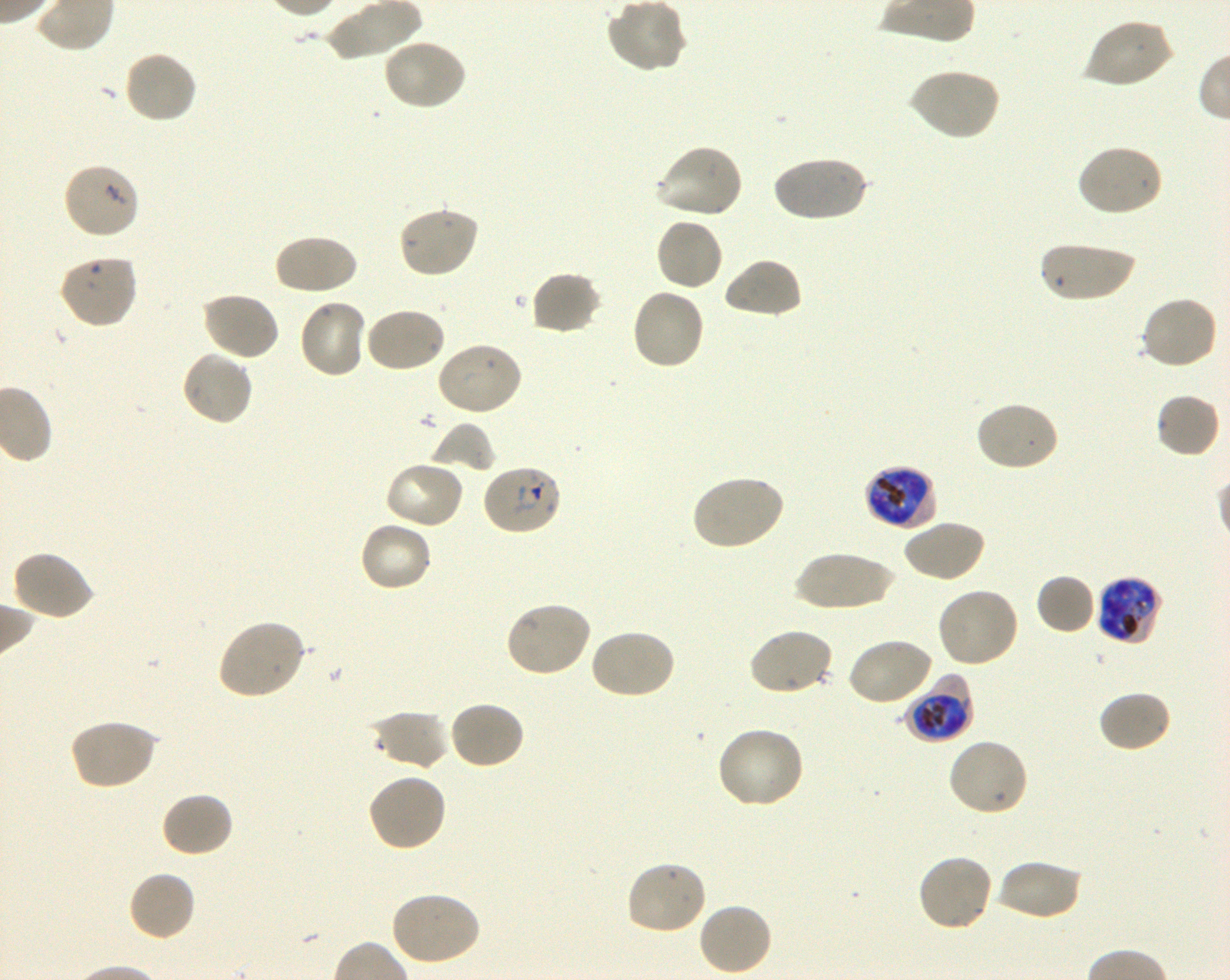

Approximate bounding rectangles given as corner coordinates in pixels from the top-left. Not every red blood cell is marked. A life-cycle stage — or a range of stages, where the recorded stages span more than one — follows each staged infected red blood cell.
Summary:
  - Locations of uninfected red blood cells: (x1=605, y1=0, x2=687, y2=73), (x1=1084, y1=17, x2=1175, y2=89), (x1=383, y1=37, x2=468, y2=111), (x1=122, y1=49, x2=199, y2=124), (x1=908, y1=68, x2=1001, y2=141), (x1=655, y1=143, x2=745, y2=220), (x1=1075, y1=143, x2=1164, y2=218), (x1=771, y1=155, x2=868, y2=223), (x1=62, y1=161, x2=141, y2=239), (x1=396, y1=204, x2=479, y2=279), (x1=654, y1=216, x2=725, y2=292), (x1=274, y1=233, x2=358, y2=296), (x1=1039, y1=241, x2=1136, y2=303), (x1=58, y1=253, x2=139, y2=329), (x1=722, y1=257, x2=804, y2=320), (x1=528, y1=270, x2=603, y2=336), (x1=630, y1=287, x2=707, y2=372), (x1=200, y1=291, x2=280, y2=362), (x1=1139, y1=295, x2=1219, y2=371), (x1=298, y1=298, x2=367, y2=379), (x1=364, y1=307, x2=447, y2=374), (x1=434, y1=341, x2=523, y2=416), (x1=180, y1=348, x2=255, y2=427), (x1=1154, y1=393, x2=1221, y2=458), (x1=973, y1=401, x2=1060, y2=473), (x1=430, y1=423, x2=496, y2=474), (x1=383, y1=460, x2=465, y2=530), (x1=691, y1=473, x2=785, y2=551), (x1=902, y1=519, x2=985, y2=583), (x1=358, y1=520, x2=434, y2=592), (x1=12, y1=549, x2=96, y2=622), (x1=792, y1=550, x2=898, y2=612), (x1=1035, y1=573, x2=1096, y2=635), (x1=935, y1=586, x2=1020, y2=669), (x1=503, y1=600, x2=593, y2=678), (x1=215, y1=618, x2=307, y2=701), (x1=588, y1=627, x2=676, y2=700), (x1=747, y1=627, x2=834, y2=696), (x1=846, y1=636, x2=934, y2=707), (x1=1097, y1=689, x2=1173, y2=754), (x1=447, y1=700, x2=526, y2=770), (x1=370, y1=710, x2=450, y2=770), (x1=68, y1=718, x2=158, y2=791), (x1=715, y1=726, x2=806, y2=811), (x1=947, y1=738, x2=1029, y2=818), (x1=366, y1=772, x2=447, y2=853), (x1=160, y1=791, x2=235, y2=859), (x1=916, y1=853, x2=994, y2=934), (x1=994, y1=858, x2=1083, y2=921), (x1=625, y1=859, x2=708, y2=936), (x1=127, y1=870, x2=196, y2=942), (x1=388, y1=891, x2=481, y2=966), (x1=698, y1=901, x2=773, y2=976)
  - Locations of infected red blood cells: (x1=482, y1=464, x2=562, y2=537) early ring to early trophozoite; (x1=863, y1=464, x2=938, y2=530) late trophozoite to early schizont; (x1=1095, y1=576, x2=1163, y2=646) late trophozoite to late schizont; (x1=903, y1=675, x2=973, y2=744) early trophozoite to early schizont
  - Objective: 100x, oil immersion, numerical aperture 1.30
  - Field of view: single
  - Stain: Giemsa
  - Culture: in-vitro Plasmodium falciparum strain 3D7, shaking
  - Donor blood group: O+
  - Image size: 1230×980 pixels
  - Preparation: thin blood film